State which parasite is depicted.
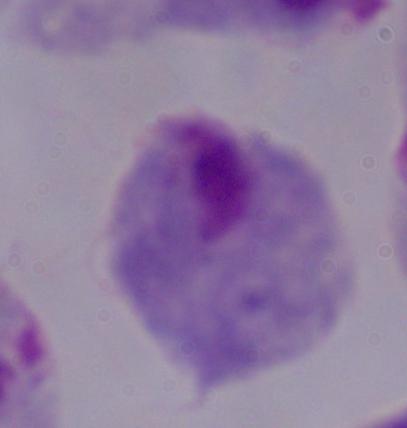

This is a trichomonad.

{
  "magnification": "1000x",
  "modality": "photomicrograph"
}